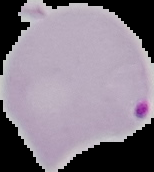

Summary:
  - Preparation: thin blood film
  - Image type: segmented cell region on a black background
  - Malaria status: parasitized
  - Image size: 154×172 pixels